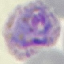

Summary:
  - Result: malaria parasites identified
  - Preparation: thin blood smear
  - Capture: smartphone camera at the microscope eyepiece
  - Image type: cell patch, automatically extracted from a larger field of view and resized to 64 × 64 pixels
  - Stain: Giemsa